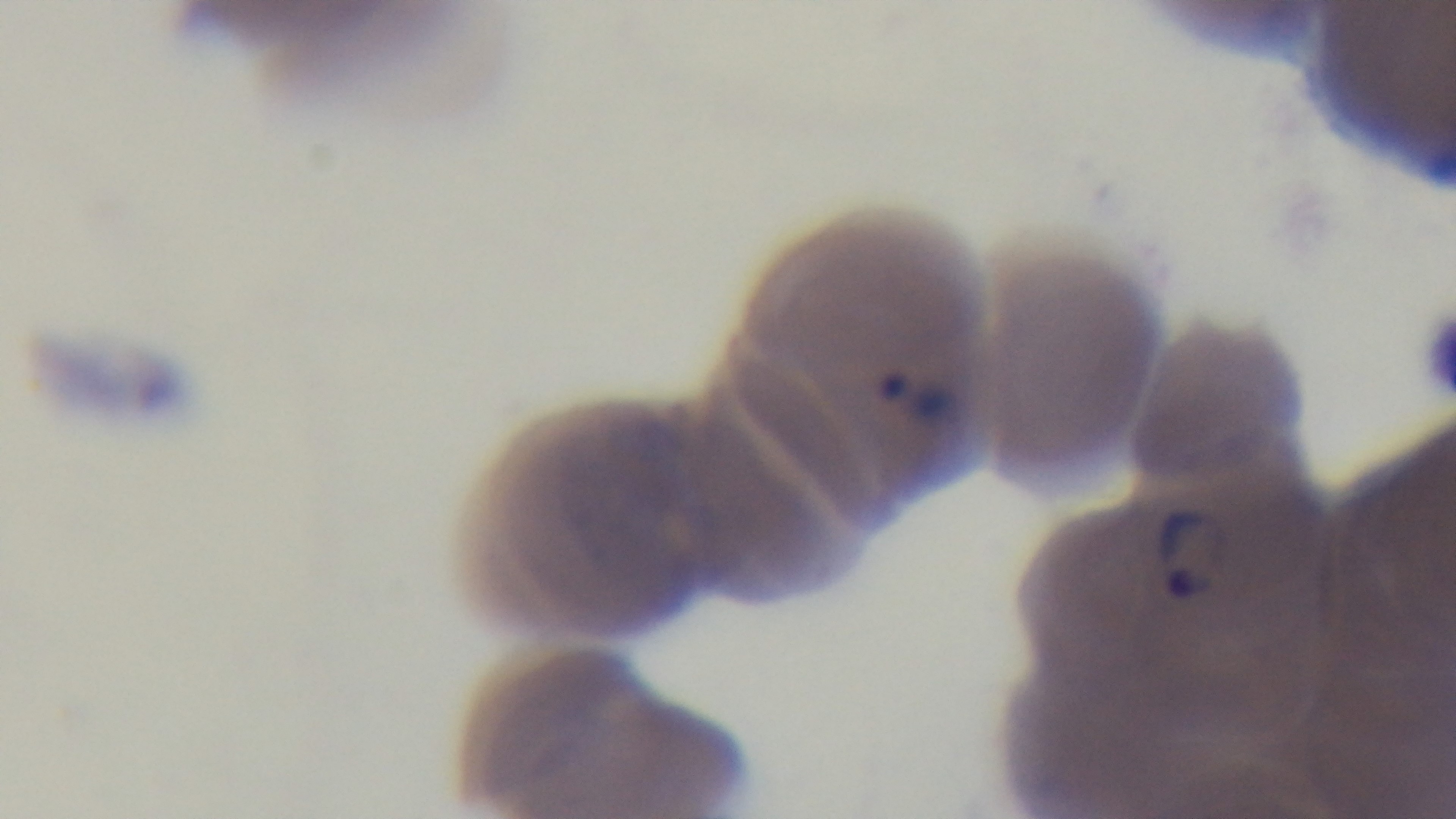

modality = light microscopy
preparation = thin
field of view = one from the slide
objective = 100x oil immersion
malaria status = infected
capture = mounted 4K digital camera
stain = Giemsa